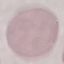
Summary:
  - Malaria status: uninfected
  - Capture: smartphone camera at the microscope eyepiece
  - Image type: automatically extracted cell patch, resized to 64 × 64 pixels
  - Stain: Giemsa
  - Preparation: thin blood film